Classify this cell by malaria status.
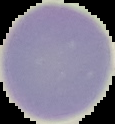
Uninfected.

Image is 115×124 pixels. Cell region segmented out of the field of view; the surrounding area is masked to black. From a thin blood film.